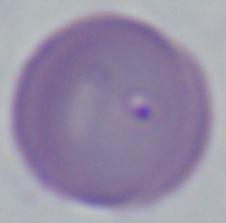

Captured at 1000x magnification. A Babesia parasite is shown. Micrograph.